Locate every Plasmodium parasite.
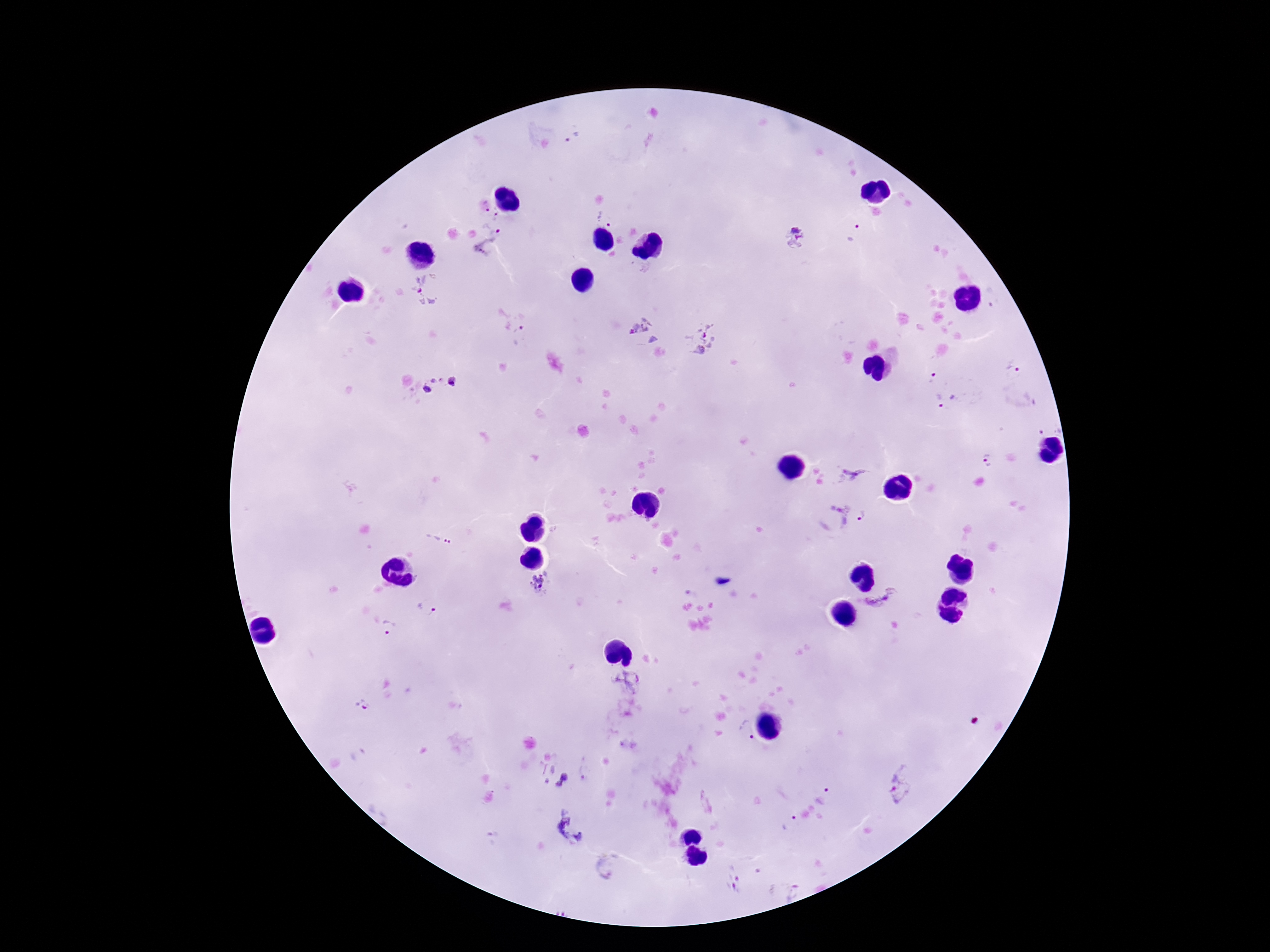

Approximate centers as [x, y] in pixels.
Plasmodium parasites: [575, 139], [484, 207], [497, 212], [605, 219], [855, 233], [795, 237], [495, 241], [638, 269], [428, 290], [644, 333], [520, 336], [702, 339], [1014, 367], [934, 376], [440, 387], [947, 399], [1050, 422], [988, 460], [851, 474], [857, 506], [440, 540], [543, 585], [883, 600], [426, 607], [390, 627], [626, 682], [365, 705], [746, 730], [585, 773], [552, 776], [903, 783], [827, 794], [788, 824], [570, 828], [610, 868], [732, 879].

stain: Giemsa
capture: smartphone camera through the microscope eyepiece
image_size: 1270×952 pixels
field_of_view: single
patient_malaria_status: infected
magnification: 100x
preparation: thick peripheral-blood smear